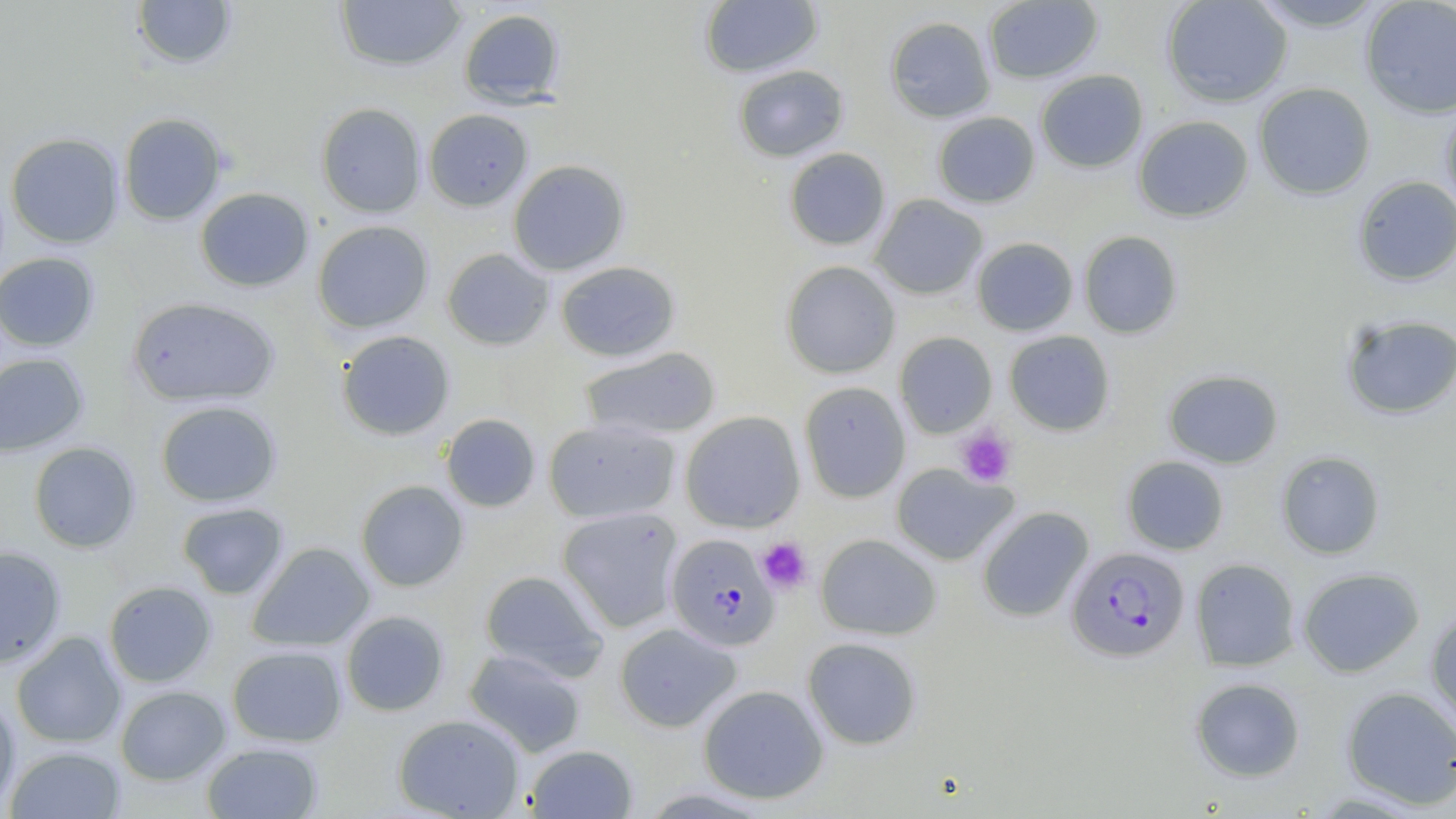
Summary:
  - Coordinate format: approximate bounding boxes as (x1,y1)-(x2,y2) corner pairs in pixels
  - Uninfected red blood cell locations: (131,0)-(237,70), (334,0)-(467,72), (700,0)-(823,78), (1161,0)-(1293,107), (1249,0)-(1388,32), (1360,0)-(1456,118), (983,1)-(1104,83), (458,8)-(565,108), (884,16)-(996,123), (732,65)-(849,162), (1035,69)-(1148,173), (1253,82)-(1375,200), (315,102)-(427,218), (1440,102)-(1456,218), (423,108)-(533,211), (932,111)-(1040,208), (118,113)-(227,225), (1133,115)-(1254,222), (6,133)-(124,248), (783,147)-(891,251), (508,159)-(630,276), (1352,176)-(1456,286), (195,187)-(314,292), (869,194)-(988,299), (312,220)-(434,333), (1078,230)-(1183,339), (971,237)-(1078,336), (441,248)-(554,351), (0,252)-(99,351), (780,260)-(900,379), (556,261)-(681,362), (126,297)-(280,407), (1340,313)-(1456,419), (336,330)-(455,440), (1004,330)-(1115,436), (894,331)-(997,438), (579,346)-(721,441), (0,353)-(89,457), (1162,369)-(1284,468), (799,382)-(910,503), (155,400)-(282,507), (680,411)-(805,533), (440,413)-(541,512), (543,418)-(681,524), (28,441)-(141,553), (1276,451)-(1385,559), (1121,455)-(1229,555), (890,463)-(1019,566), (355,480)-(469,592), (177,502)-(289,600), (556,506)-(685,633), (976,506)-(1094,622), (816,534)-(941,640), (246,542)-(375,652), (0,546)-(66,668), (1190,557)-(1301,671), (1297,567)-(1425,677), (479,569)-(609,681), (103,581)-(217,687), (1426,609)-(1456,729), (340,610)-(449,716), (614,622)-(741,732), (11,631)-(127,748), (802,636)-(923,750), (227,645)-(348,747), (464,649)-(587,758), (1189,677)-(1305,782), (698,684)-(829,804), (115,685)-(231,785), (1341,687)-(1456,810), (0,694)-(20,812), (393,714)-(525,818), (201,742)-(323,818), (524,744)-(638,818), (5,745)-(127,818)
  - Plasmodium falciparum-infected red blood cell locations: (666,533)-(780,651), (1066,546)-(1189,662)
  - Platelet locations: (956,426)-(1017,488), (756,537)-(812,593)
  - Slide-level diagnosis: Plasmodium falciparum
  - Modality: optical microscopy
  - Image size: 1456×819 pixels
  - Stain: May-Grünwald-Giemsa
  - Magnification: 1000x
  - Preparation: thin blood film
  - Field of view: one of a larger specimen